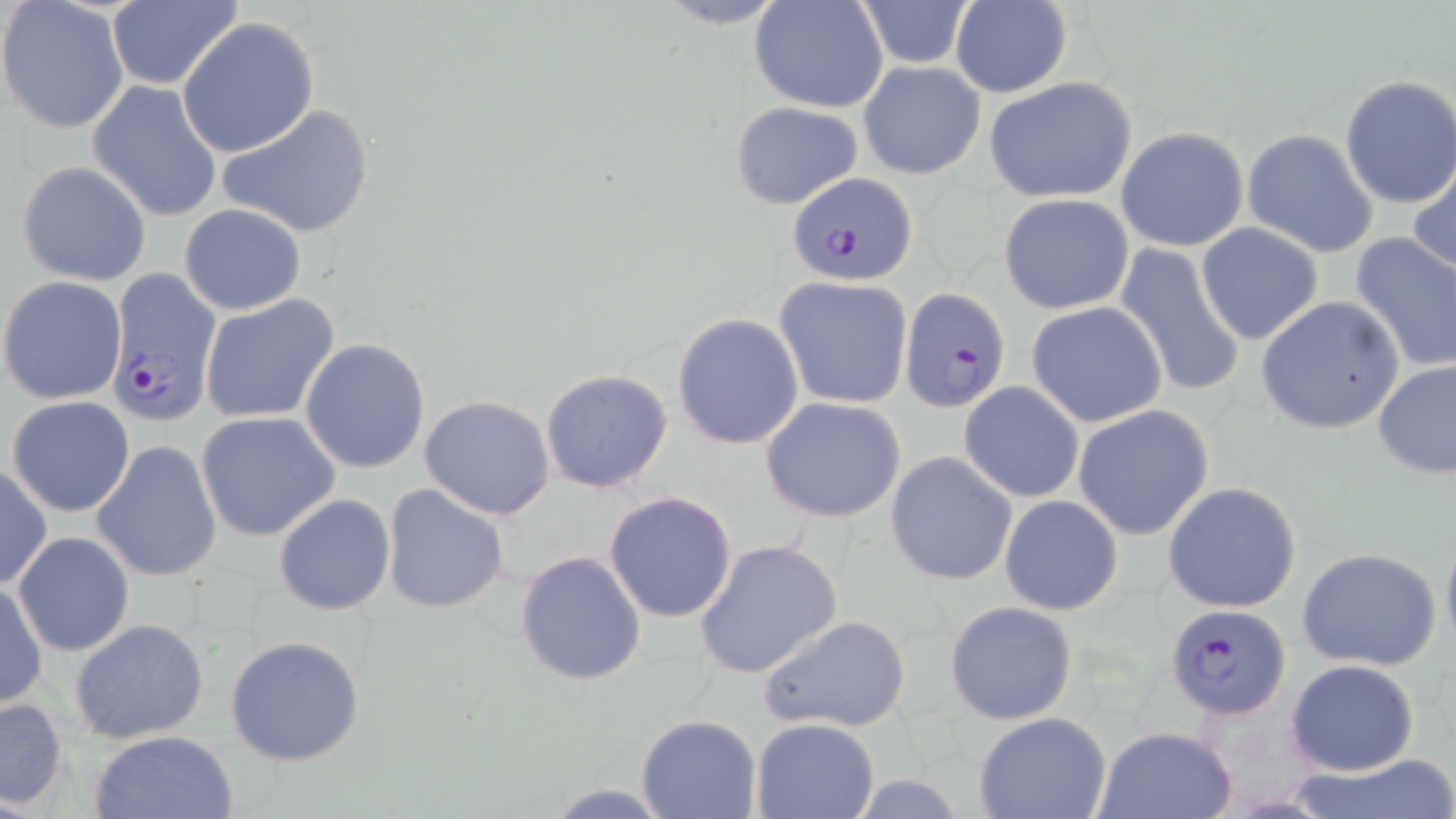

Summary:
  - Coordinate format: approximate bounding boxes as (x1, y1, x2, y2) in pixels
  - Uninfected red blood cell locations (subset): (647, 0, 798, 29), (851, 0, 977, 69), (950, 0, 1072, 97), (0, 1, 130, 136), (749, 1, 889, 114), (104, 2, 242, 90), (176, 17, 319, 159), (857, 60, 985, 180), (984, 75, 1138, 203), (1337, 75, 1455, 210), (86, 81, 223, 222), (730, 101, 863, 211), (216, 102, 376, 239), (1115, 126, 1249, 252), (1242, 129, 1381, 259), (1409, 158, 1456, 280), (15, 161, 151, 285), (998, 192, 1134, 314), (178, 204, 307, 316), (1196, 223, 1323, 346), (1350, 232, 1456, 372), (1114, 243, 1246, 400), (0, 274, 128, 405), (774, 276, 914, 410), (199, 294, 341, 424), (1256, 295, 1407, 436), (1026, 300, 1169, 428), (672, 313, 804, 450), (299, 338, 430, 474), (1373, 359, 1455, 480), (539, 369, 673, 494), (959, 380, 1084, 503), (8, 395, 135, 517), (418, 395, 556, 519), (761, 396, 907, 524), (1073, 405, 1216, 541), (195, 411, 340, 541), (90, 440, 222, 582), (884, 451, 1017, 587), (0, 464, 50, 590), (1162, 481, 1303, 614), (381, 484, 509, 614), (604, 490, 737, 622), (998, 493, 1123, 614), (274, 494, 397, 615), (1439, 523, 1456, 663), (12, 533, 135, 656), (693, 538, 842, 680), (1298, 547, 1443, 672), (514, 549, 647, 687), (1, 581, 48, 710), (943, 599, 1078, 724), (757, 614, 912, 735), (69, 619, 210, 744), (223, 634, 366, 768), (1285, 659, 1420, 777), (1, 697, 70, 811), (636, 713, 762, 818), (972, 713, 1112, 819), (751, 718, 878, 819), (1094, 726, 1239, 819), (90, 730, 239, 818), (1286, 753, 1455, 819), (541, 782, 676, 816)
  - Plasmodium falciparum-infected red blood cell locations (subset): (788, 170, 921, 284), (898, 284, 1010, 412), (1165, 602, 1292, 720)
  - Slide-level diagnosis: Plasmodium falciparum
  - Preparation: thin blood film
  - Field of view: single
  - Modality: light microscopy
  - Magnification: 1000x
  - Image size: 1456×819 pixels
  - Stain: May-Grünwald-Giemsa